Describe the morphology of the red blood cells.
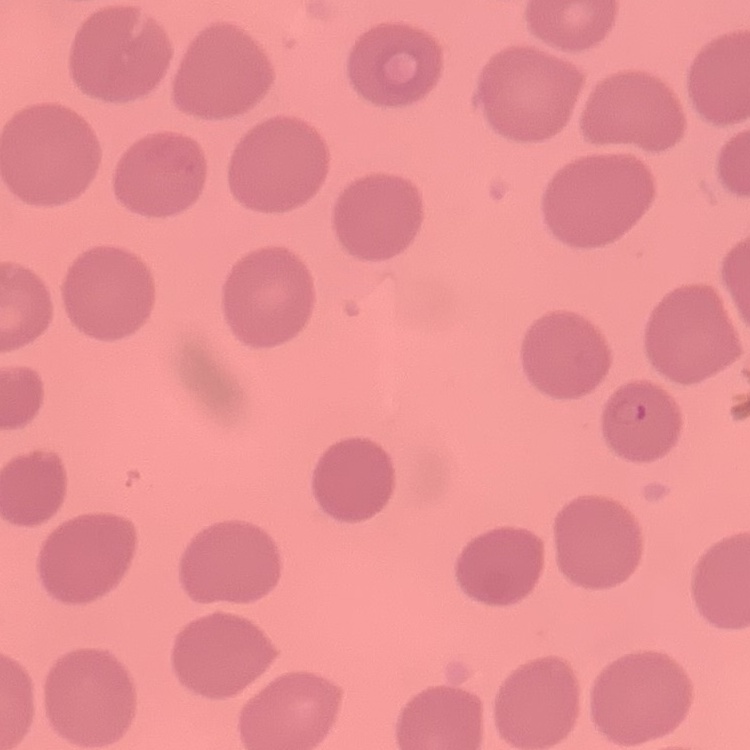
No rouleaux formation.

Summary:
  - Preparation: thin blood smear
  - Stain: Field's or Giemsa
  - Image type: square crop of a larger photomicrograph